Locate every leukocyte (white blood cell).
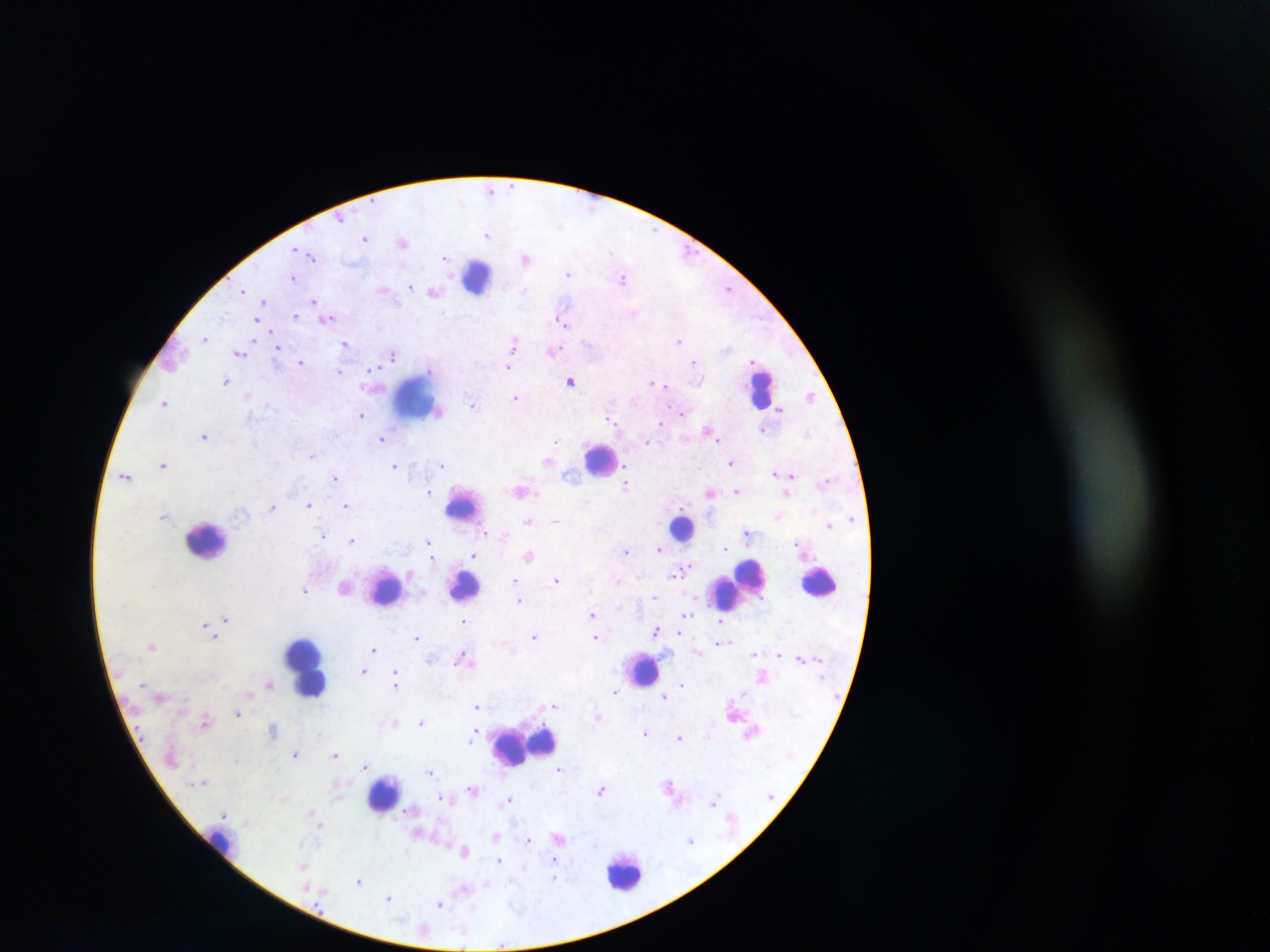

Approximate centers as x y in pixels.
Leukocytes: 479 277; 762 388; 415 398; 600 459; 461 509; 682 527; 206 540; 822 582; 737 584; 465 585; 387 590; 305 666; 643 669; 525 745; 384 794; 221 842; 626 871.

Plasmodium parasite locations: 512 185; 490 189; 341 219; 558 225; 653 230; 487 234; 364 237; 402 241; 296 249; 611 251; 688 252; 311 255; 444 257; 525 257; 569 274; 293 277; 623 279; 410 287; 728 288; 243 290; 383 290; 425 290; 525 290; 433 292; 314 301; 264 302; 443 312; 634 314; 296 316; 327 319; 256 321; 562 321; 205 338; 679 340; 514 342; 345 343; 278 348; 554 350; 239 353; 394 354; 754 360; 694 361; 301 362; 508 367; 372 369; 340 371; 226 381; 571 381; 652 383; 659 384; 666 386; 810 395; 247 396; 515 398; 165 401; 473 405; 780 409; 682 413; 361 415; 611 419; 661 423; 706 429; 763 430; 204 436; 382 439; 646 440; 719 440; 555 441; 312 455; 547 461; 731 463; 163 465; 394 465; 443 465; 626 465; 775 473; 568 474; 791 474; 126 475; 627 475; 335 479; 627 484; 429 491; 522 491; 736 491; 710 493; 787 493; 309 505; 345 505; 272 506; 163 516; 555 520; 529 521; 828 525; 485 533; 746 533; 323 536; 503 536; 351 540; 428 542; 796 542; 726 548; 659 549; 626 551; 473 555; 529 555; 431 556; 682 571; 556 579; 515 580; 618 580; 305 590; 654 597; 518 600; 592 613; 686 615; 225 618; 463 621; 204 624; 720 624; 656 630; 679 633; 534 636; 595 636; 417 637; 215 638; 729 641; 720 643; 152 647; 373 648; 697 651; 755 653; 779 654; 461 657; 801 657; 364 671; 396 676; 396 683; 269 684; 682 684; 615 692; 664 697; 555 706; 477 707; 238 713; 205 721; 395 722; 421 722; 273 729; 645 733; 473 735; 679 737; 472 740; 295 754; 335 754; 366 766; 558 769; 430 772; 203 782; 473 789; 601 790; 441 797; 508 799; 713 802; 223 813; 312 813; 320 825; 495 836; 559 838; 529 840; 691 840; 465 851; 407 853; 499 860; 553 860; 303 866; 555 877; 359 881; 487 885; 464 890; 389 898; 440 904; 501 945. Photographed through a microscope with a mobile-phone camera. Image is 1270×952 pixels. Sample from Ghana. Single field of view. Thick blood smear.